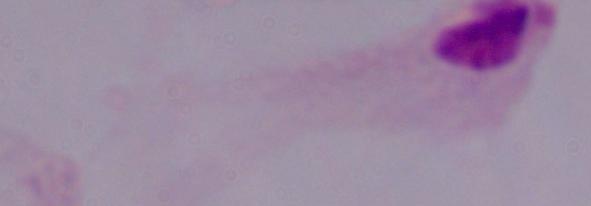
modality: micrograph
magnification: 1000x
identification: trichomonad